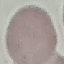

{
  "result": "no malaria parasites detected",
  "image_type": "cell patch, automatically extracted from a larger field of view and resized to 64 × 64 pixels",
  "capture": "smartphone camera at the microscope eyepiece",
  "stain": "Giemsa",
  "preparation": "thin blood smear"
}